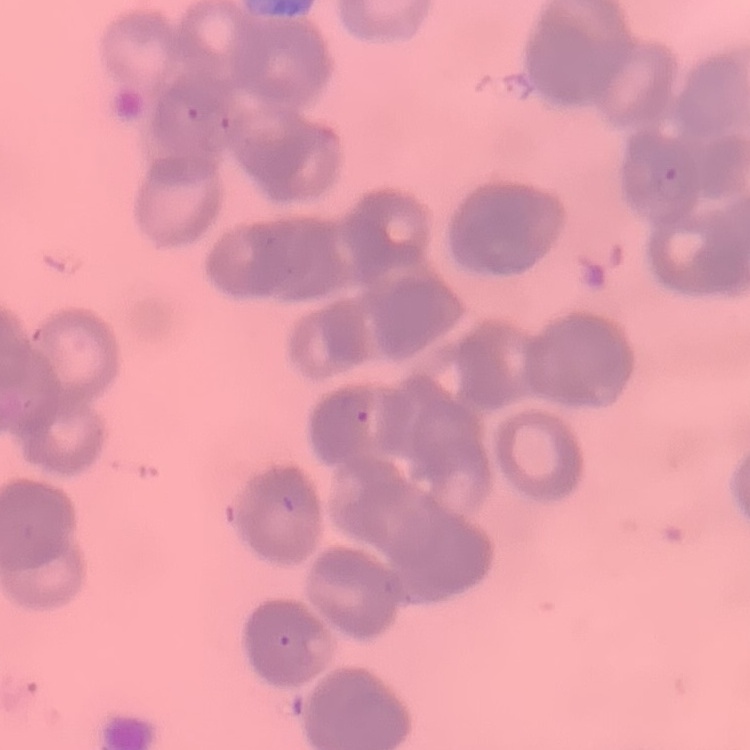

Summary:
  - Red blood cell morphology: rouleaux formation
  - Preparation: thin peripheral smear
  - Image type: one tile cut from a larger photomicrograph
  - Stain: Field's or Giemsa